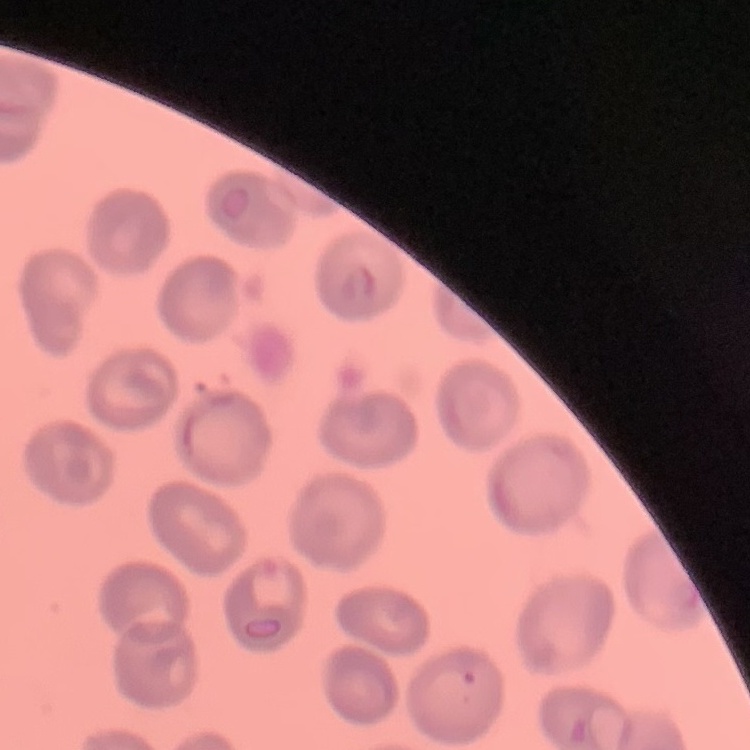
Summary:
  - Erythrocyte morphology: no rouleaux formation
  - Preparation: thin blood smear
  - Stain: Field's or Giemsa
  - Image type: one tile cut from a larger photomicrograph